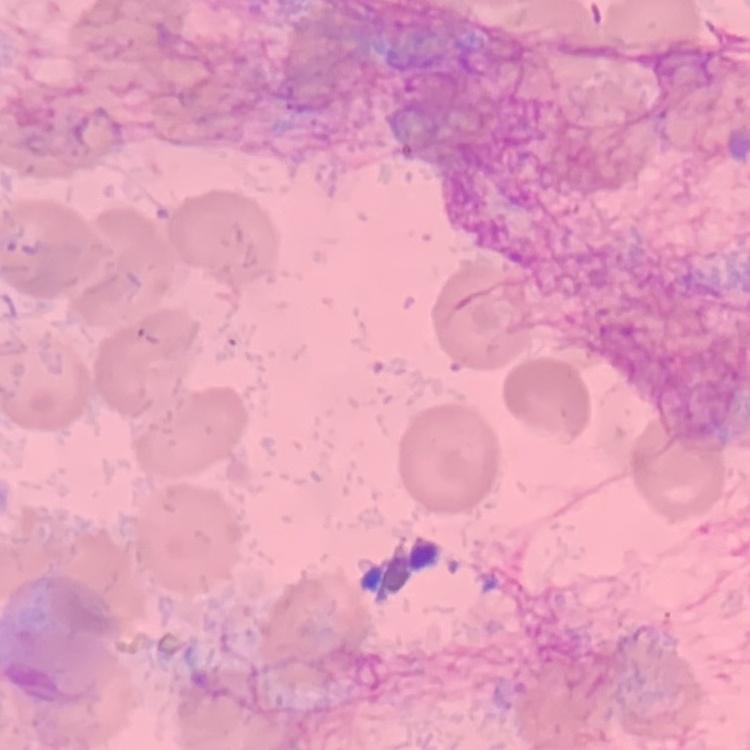
red blood cell morphology = no rouleaux formation
preparation = thin blood smear
stain = Field's or Giemsa
image type = square crop of a larger photomicrograph